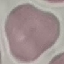
Summary:
  - Malaria status: uninfected
  - Preparation: thin blood smear
  - Image type: automatically extracted cell patch, resized to 64 × 64 pixels
  - Stain: Giemsa
  - Capture: smartphone camera at the microscope eyepiece